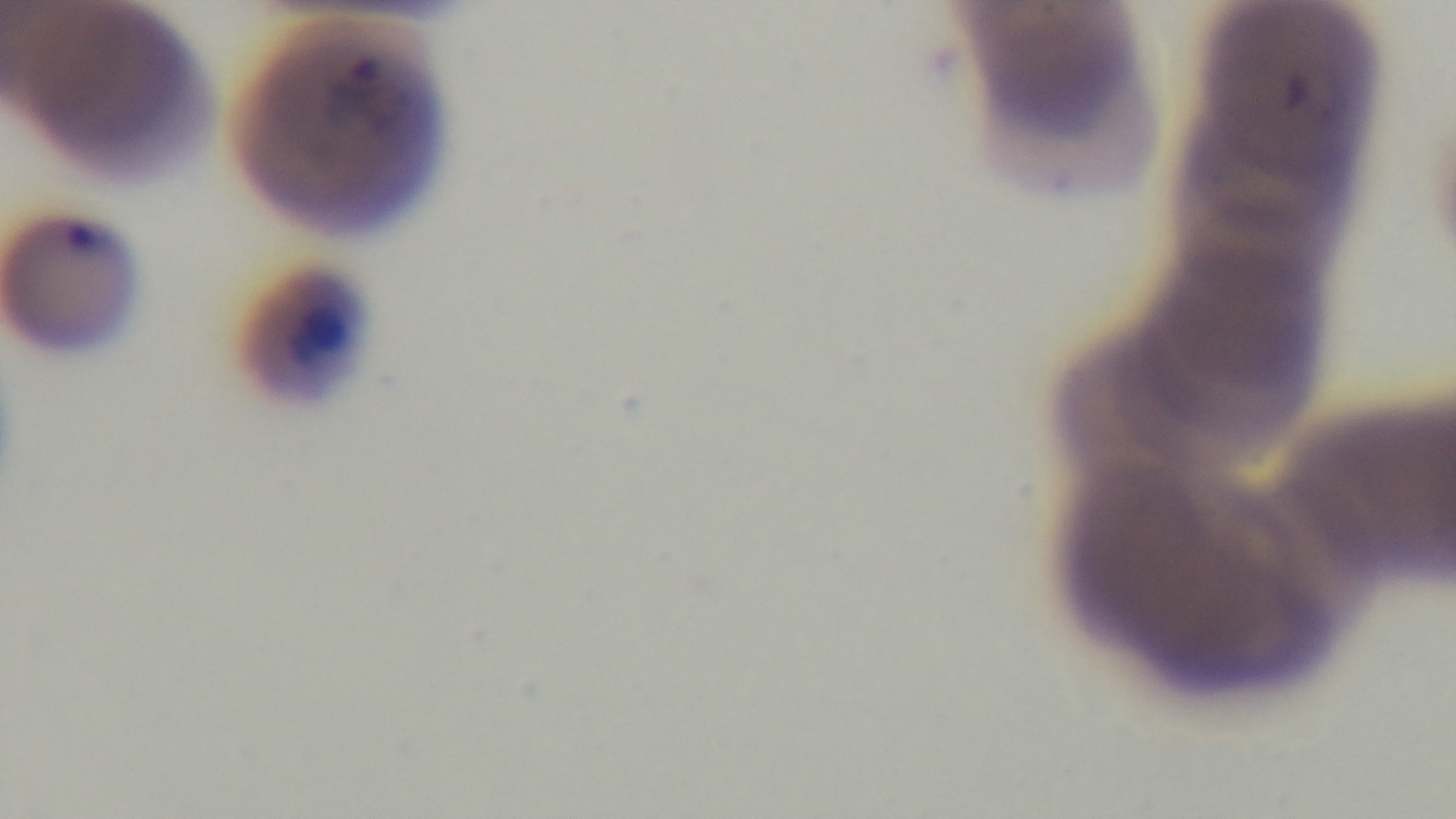
Light microscopy. Malaria status: infected. Giemsa-stained. Preparation: thin smear. One field from the slide. Captured with a mounted 4K digital camera. Oil-immersion objective, 100x.